Classify this cell by malaria status.
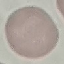
It is uninfected.

{
  "capture": "smartphone camera at the microscope eyepiece",
  "image_type": "cell patch, automatically extracted from a larger field of view and resized to 64 × 64 pixels",
  "preparation": "thin blood film",
  "stain": "Giemsa"
}